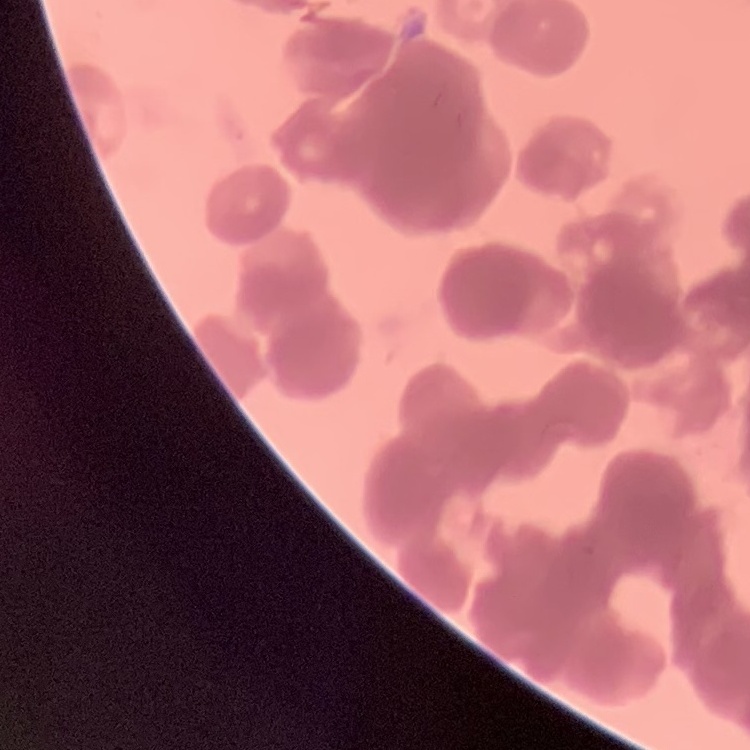

{
  "erythrocyte_morphology": "rouleaux formation",
  "preparation": "thin peripheral smear",
  "stain": "Field's or Giemsa",
  "image_type": "one tile cut from a larger photomicrograph"
}